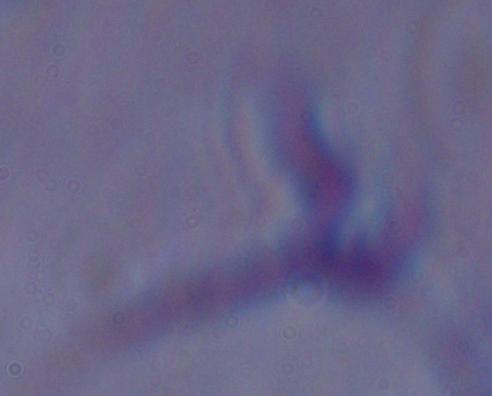 Captured at 1000x magnification. Micrograph. A trypanosome is shown.